Locate every Plasmodium parasite.
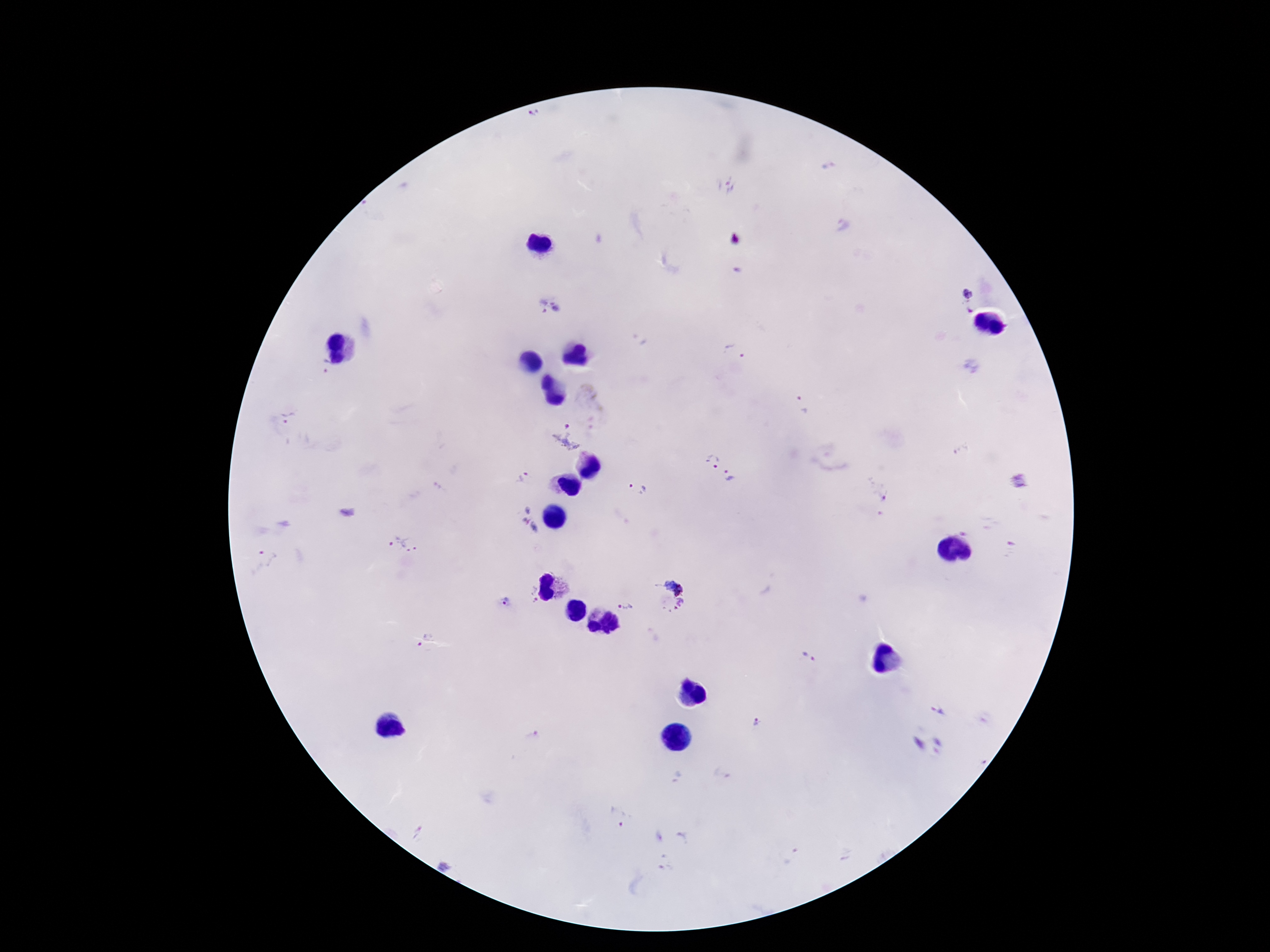

Approximate centers as (x, y) in pixels.
Plasmodium parasites: (734, 240), (967, 302), (549, 305), (735, 354), (800, 404), (288, 418), (566, 434), (712, 461), (729, 477), (519, 479), (1023, 483), (638, 489), (528, 518), (400, 545), (263, 559), (673, 586), (530, 595), (506, 602), (680, 604), (625, 606), (423, 642), (808, 657), (939, 711), (758, 722), (930, 744), (616, 816).

Summary:
  - Image size: 1270×952 pixels
  - Patient malaria status: infected
  - Magnification: 100x
  - Field of view: single
  - Preparation: thick blood smear
  - Stain: Giemsa
  - Capture: smartphone camera through the microscope eyepiece